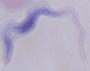

modality = micrograph
identification = trypanosome
magnification = 1000x